Name the parasite shown.
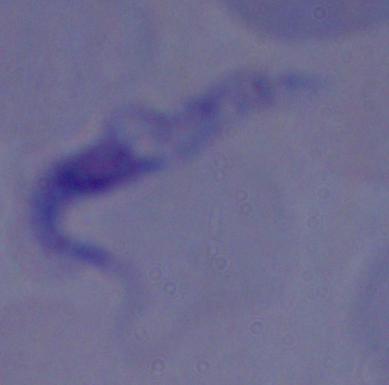

This is a trypanosome.

1000x magnification. Micrograph.